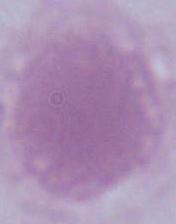

modality = photomicrograph
magnification = 1000x
identification = red blood cell